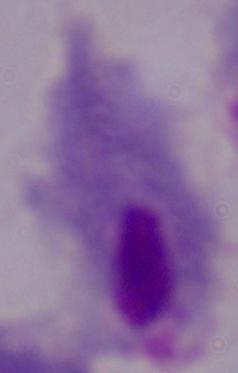
Summary:
  - Magnification: 1000x
  - Modality: micrograph
  - Identification: trichomonad